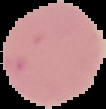

image size = 106×109 pixels
malaria status = uninfected
image type = cell region segmented out of the field of view; surrounding area masked to black
preparation = thin blood film